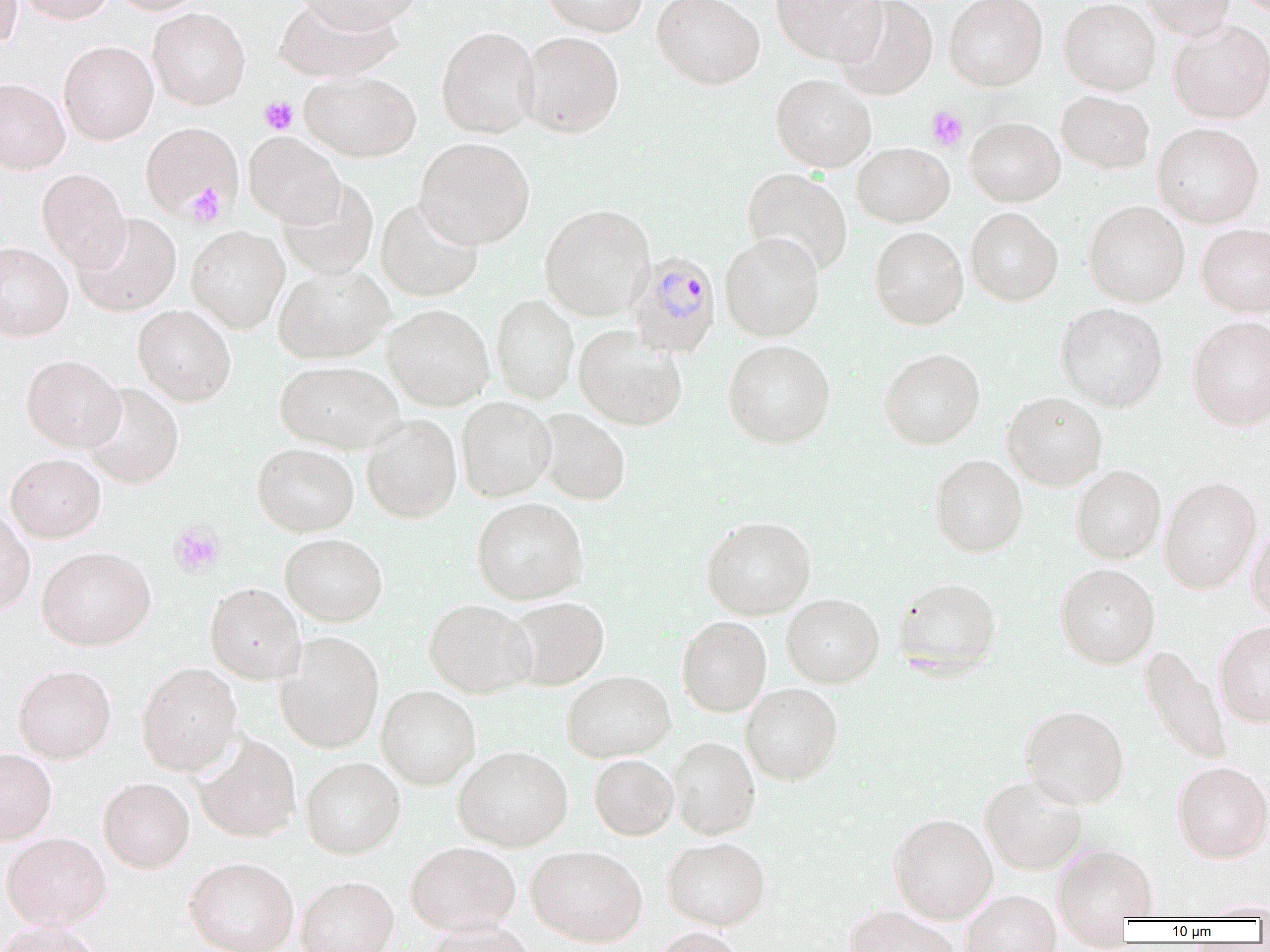

Summary:
  - Coordinate format: approximate bounding boxes as (x1, y1, x2, y2) in pixels
  - Uninfected red blood cell locations: (0, 0, 23, 50), (18, 0, 114, 24), (110, 0, 206, 15), (293, 0, 423, 33), (540, 0, 648, 36), (653, 0, 765, 90), (771, 0, 886, 65), (834, 0, 938, 100), (943, 0, 1047, 91), (1059, 0, 1160, 95), (1141, 0, 1236, 41), (275, 1, 402, 82), (148, 7, 250, 109), (1167, 20, 1270, 124), (436, 26, 540, 139), (517, 31, 624, 138), (58, 41, 158, 144), (299, 71, 421, 162), (771, 74, 876, 173), (0, 78, 70, 174), (1056, 90, 1154, 173), (965, 117, 1065, 206), (141, 121, 241, 219), (1152, 122, 1264, 228), (244, 133, 345, 227), (414, 137, 535, 248), (851, 142, 954, 227), (743, 167, 852, 276), (37, 169, 130, 270), (277, 179, 379, 280), (376, 198, 484, 301), (1083, 200, 1189, 307), (539, 204, 655, 321), (965, 207, 1063, 306), (72, 212, 181, 316), (1196, 223, 1270, 317), (186, 226, 289, 333), (869, 226, 968, 330), (720, 232, 825, 341), (0, 242, 73, 340), (273, 265, 393, 363), (491, 294, 579, 403), (1056, 303, 1168, 412), (383, 304, 494, 411), (133, 305, 236, 406), (1187, 315, 1270, 431), (574, 325, 687, 431), (722, 339, 836, 448), (879, 347, 985, 449), (22, 354, 124, 452), (274, 360, 403, 453), (81, 383, 184, 488), (1002, 391, 1107, 490), (456, 397, 556, 501), (534, 408, 631, 505), (361, 414, 461, 523), (252, 443, 359, 536), (6, 453, 106, 543), (929, 454, 1028, 557), (1070, 464, 1165, 563), (1159, 476, 1262, 594), (471, 497, 589, 605), (0, 508, 35, 616), (701, 516, 816, 620), (1246, 522, 1270, 622), (280, 533, 387, 626), (37, 545, 156, 651), (1054, 563, 1160, 669), (891, 576, 1002, 676), (205, 583, 305, 684), (782, 593, 884, 688), (504, 596, 609, 690), (424, 599, 535, 698), (677, 616, 771, 716), (1213, 620, 1270, 727), (275, 631, 384, 753), (1141, 645, 1231, 765), (136, 662, 242, 775), (13, 663, 116, 763), (561, 669, 676, 762), (740, 682, 843, 785), (376, 685, 481, 790), (1020, 704, 1129, 809), (192, 733, 302, 843), (667, 736, 760, 840), (453, 745, 573, 851), (0, 747, 57, 844), (589, 754, 679, 840), (300, 756, 405, 859), (1171, 760, 1270, 863), (979, 775, 1089, 874), (98, 777, 195, 873), (888, 812, 998, 923), (1, 831, 111, 929), (662, 837, 770, 930), (405, 840, 520, 934), (526, 844, 648, 947), (1053, 844, 1158, 921), (183, 855, 299, 952), (296, 875, 398, 952), (959, 890, 1062, 952), (843, 905, 960, 952), (0, 918, 102, 952), (424, 919, 541, 951), (652, 926, 748, 952)
  - Platelet locations: (260, 97, 298, 134), (925, 106, 968, 151), (183, 183, 228, 227), (168, 521, 225, 577)
  - Plasmodium malariae-infected red blood cell locations: (627, 250, 722, 358)
  - Slide-level diagnosis: Plasmodium malariae
  - Field of view: one of a larger specimen
  - Preparation: thin blood film
  - Modality: optical microscopy
  - Magnification: 1000x
  - Image size: 1270×952 pixels